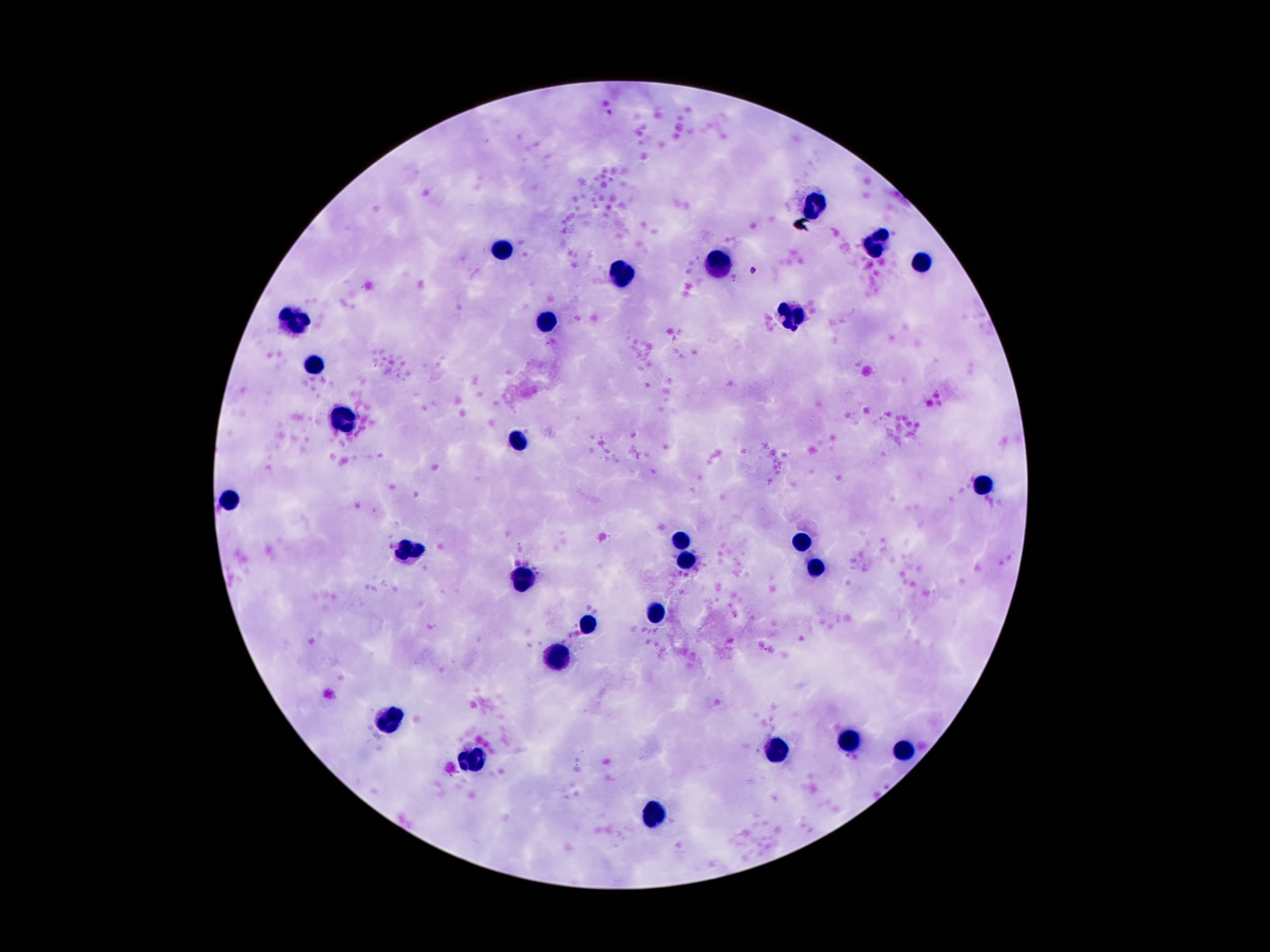
Approximate object centers, in pixels from the top-left corner.
Summary:
  - Leukocyte locations: (x=816, y=201), (x=873, y=243), (x=500, y=249), (x=924, y=262), (x=717, y=264), (x=623, y=274), (x=791, y=315), (x=293, y=317), (x=545, y=321), (x=314, y=365), (x=344, y=417), (x=517, y=440), (x=982, y=483), (x=230, y=498), (x=681, y=544), (x=803, y=544), (x=410, y=550), (x=685, y=561), (x=812, y=565), (x=521, y=581), (x=654, y=613), (x=586, y=622), (x=555, y=657), (x=389, y=721), (x=851, y=740), (x=775, y=746), (x=906, y=748), (x=471, y=762), (x=654, y=809)
  - Image size: 1270×952 pixels
  - Magnification: 100x
  - Patient malaria status: not infected
  - Preparation: thick peripheral-blood smear
  - Stain: Giemsa
  - Capture: smartphone camera through the microscope eyepiece
  - Field of view: single